Outline each blood parasite and name the species.
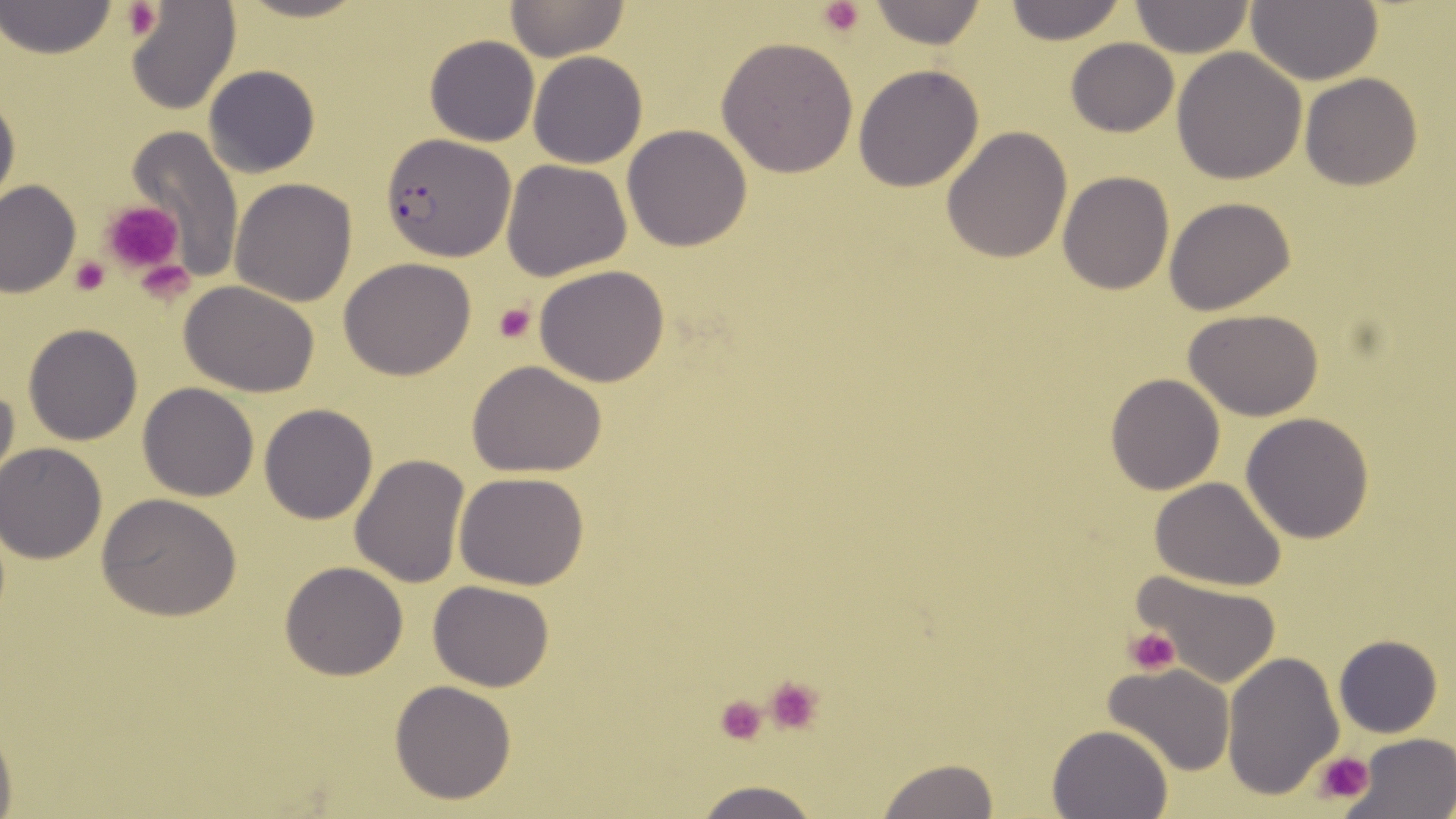
Approximate bounding boxes as (x1, y1, x2, y2) in pixels.
Plasmodium falciparum-infected red blood cells: (380, 135, 514, 259).
No Plasmodium ovale, Plasmodium malariae, Plasmodium vivax, Babesia divergens, or Trypanosoma brucei observed.

Summary:
  - Uninfected red blood cell locations: (231, 0, 375, 25), (505, 0, 630, 61), (864, 0, 989, 49), (1000, 0, 1130, 46), (1247, 0, 1384, 86), (1, 2, 117, 60), (125, 2, 242, 115), (1129, 2, 1254, 58), (424, 34, 540, 146), (716, 36, 860, 178), (1065, 38, 1178, 137), (1172, 47, 1306, 184), (528, 51, 648, 169), (203, 64, 320, 177), (853, 64, 985, 192), (1300, 72, 1421, 190), (0, 83, 19, 218), (621, 124, 752, 250), (126, 125, 244, 278), (941, 127, 1072, 264), (501, 158, 632, 281), (1057, 171, 1174, 294), (231, 178, 358, 306), (1, 181, 79, 297), (1164, 198, 1296, 315), (339, 257, 477, 380), (535, 266, 671, 387), (178, 280, 320, 396), (1186, 310, 1324, 421), (23, 324, 143, 444), (467, 361, 608, 477), (0, 372, 19, 498), (1105, 372, 1226, 495), (137, 383, 260, 501), (259, 402, 379, 524), (1240, 412, 1374, 543), (0, 443, 106, 564), (349, 454, 471, 590), (455, 473, 588, 589), (1150, 476, 1288, 591), (98, 493, 242, 621), (280, 563, 407, 680), (1132, 568, 1283, 686), (429, 579, 556, 691), (1335, 634, 1441, 737), (1223, 651, 1344, 800), (1103, 664, 1236, 776), (389, 680, 518, 805), (0, 716, 17, 819), (1048, 724, 1173, 819), (1354, 733, 1455, 817), (877, 757, 1001, 818), (686, 779, 828, 819)
  - Platelet locations: (820, 0, 864, 38), (122, 2, 162, 42), (102, 200, 186, 276), (68, 256, 109, 296), (493, 302, 536, 344), (1124, 627, 1180, 674), (763, 674, 828, 736), (713, 693, 770, 746), (1314, 749, 1374, 806)
  - Slide-level diagnosis: Plasmodium falciparum
  - Modality: optical microscopy
  - Magnification: 1000x
  - Image size: 1456×819 pixels
  - Stain: May-Grünwald-Giemsa
  - Field of view: one of a larger specimen
  - Preparation: thin blood film